Report the malaria status of this cell.
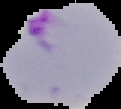
It is parasitized.

preparation = thin blood smear
image type = segmented cell region with the area outside set to black
image size = 121×109 pixels